Give the extent of all uninfected red blood cells.
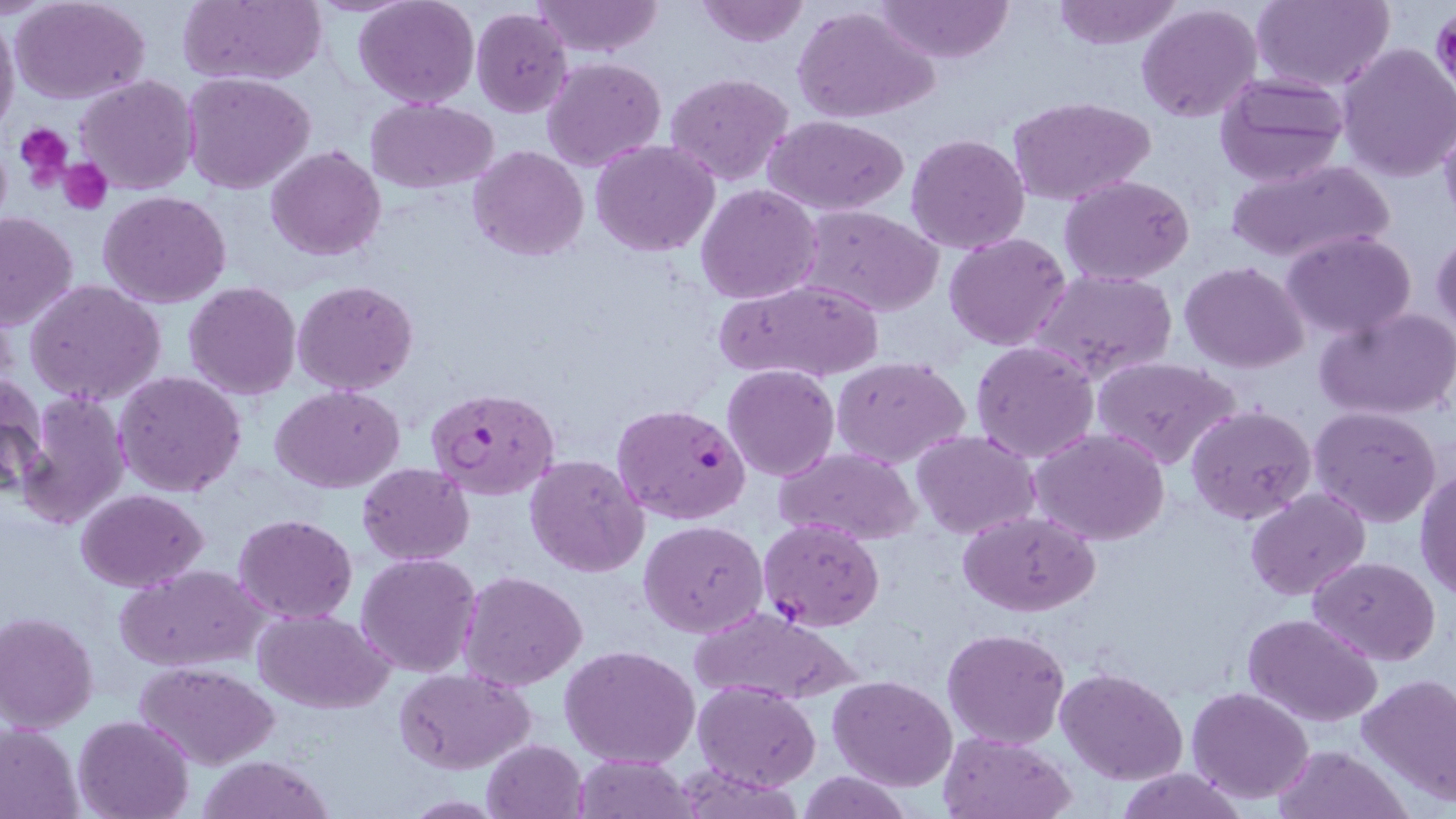

Approximate bounding boxes as (x1,y1)-(x2,y2) corner pairs in pixels.
Uninfected red blood cells: (10,0)-(151,104), (177,0)-(325,87), (355,0)-(478,108), (531,0)-(663,57), (693,0)-(811,48), (877,0)-(1013,64), (1050,0)-(1184,50), (1251,0)-(1394,91), (1137,3)-(1263,123), (791,4)-(940,126), (471,7)-(574,117), (0,12)-(20,139), (1335,41)-(1456,182), (542,57)-(666,172), (183,71)-(316,193), (667,72)-(793,187), (1213,72)-(1349,188), (75,74)-(199,194), (1008,96)-(1155,204), (365,97)-(498,193), (1439,114)-(1456,230), (763,115)-(911,217), (906,133)-(1030,253), (590,140)-(721,257), (266,145)-(385,261), (468,145)-(590,262), (1225,157)-(1396,265), (1059,175)-(1196,285), (696,183)-(823,303), (99,191)-(231,309), (799,204)-(946,318), (0,211)-(79,332), (1282,230)-(1418,339), (1431,231)-(1455,341), (944,233)-(1072,351), (1179,261)-(1310,372), (1033,269)-(1177,388), (713,277)-(885,385), (24,280)-(169,407), (292,280)-(418,395), (183,281)-(302,401), (1315,306)-(1456,420), (970,340)-(1100,463), (831,356)-(971,469), (1091,356)-(1242,472), (722,364)-(839,482), (1,371)-(48,500), (115,371)-(247,497), (270,386)-(404,493), (12,391)-(133,530), (1186,404)-(1316,525), (1308,406)-(1444,529), (1030,428)-(1174,548), (911,430)-(1040,540), (775,448)-(923,544), (524,453)-(650,577), (356,462)-(475,565), (1415,467)-(1456,600), (1244,488)-(1369,601), (77,489)-(208,592), (959,512)-(1099,617), (233,514)-(359,623), (639,520)-(768,637), (356,552)-(482,677), (1308,557)-(1441,666), (119,564)-(268,672), (459,571)-(588,692), (688,605)-(864,707), (254,610)-(393,712), (1,611)-(99,732), (1243,611)-(1385,727), (941,627)-(1071,748), (1299,628)-(1455,770), (559,644)-(702,769), (136,661)-(279,768), (1056,666)-(1188,785), (394,667)-(535,774), (829,675)-(957,791), (1358,675)-(1456,805), (693,681)-(821,790), (1186,685)-(1314,803), (73,714)-(194,819), (0,721)-(84,819), (937,731)-(1075,818), (483,738)-(588,817), (1272,745)-(1409,819), (574,754)-(697,819), (194,755)-(338,819), (1115,767)-(1247,819), (796,771)-(912,818).

slide-level diagnosis = Plasmodium falciparum
image size = 1456×819 pixels
field of view = one of a larger specimen
magnification = 1000x
platelet locations = approximate bounding boxes as (x1,y1)-(x2,y2) corner pairs in pixels: (1432,9)-(1456,90), (15,123)-(72,187), (59,157)-(112,215)
modality = light microscopy
stain = May-Grünwald-Giemsa
Plasmodium falciparum-infected red blood cell locations = approximate bounding boxes as (x1,y1)-(x2,y2) corner pairs in pixels: (428,387)-(561,500), (612,402)-(751,524), (759,519)-(884,631)
preparation = thin blood smear